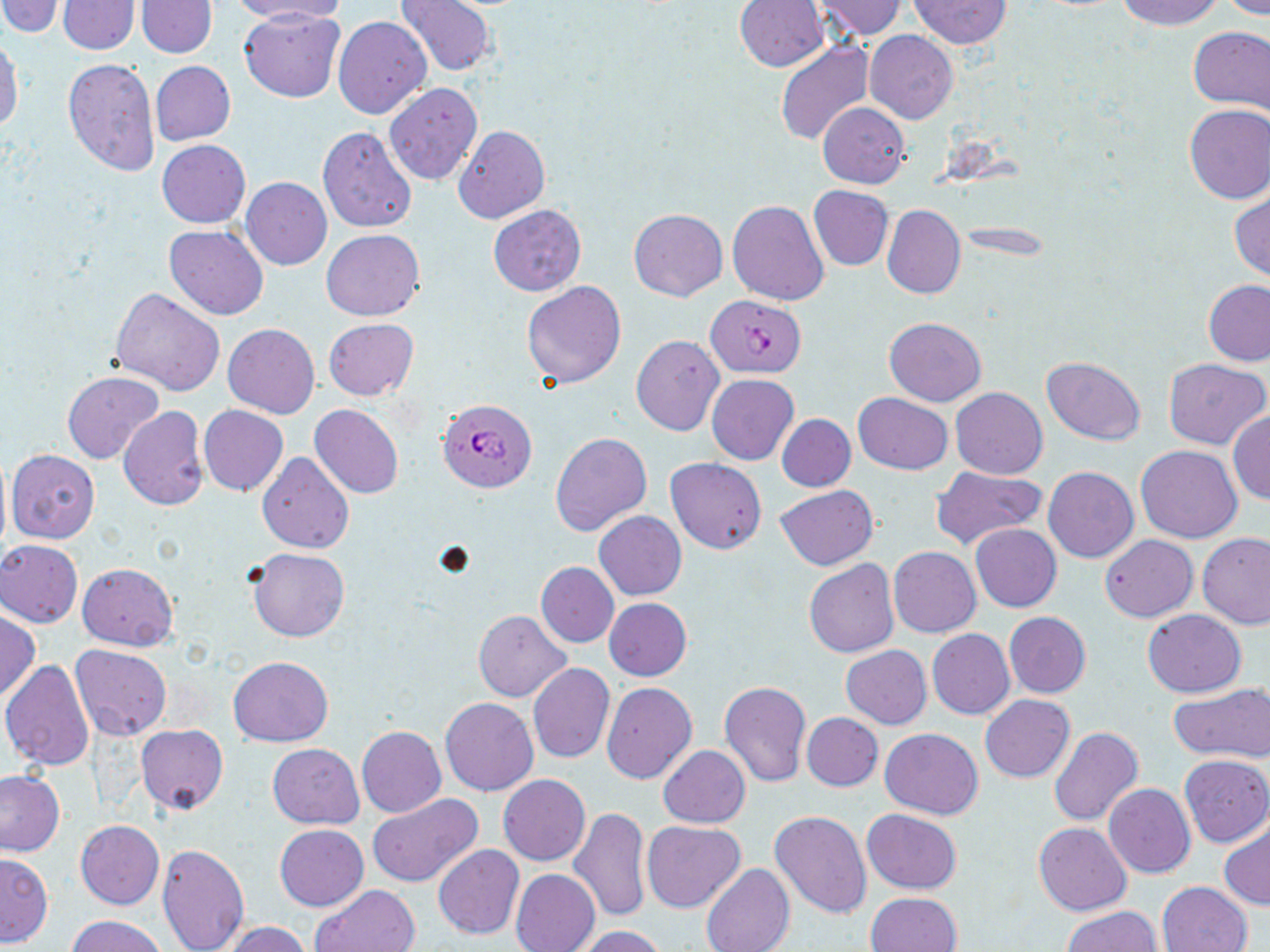
slide_level_diagnosis: Plasmodium falciparum
stain: May-Grünwald-Giemsa
uninfected_red_blood_cell_locations: 'approximate bounding boxes as (x1,y1)-(x2,y2) corner pairs in pixels: (0,0)-(65,37), (137,0)-(216,57), (233,0)-(350,24), (394,0)-(495,77), (811,0)-(906,40), (907,0)-(1012,49), (1117,0)-(1222,29), (1219,0)-(1270,19), (56,1)-(141,54), (735,1)-(828,72), (238,6)-(345,102), (333,15)-(432,119), (1188,25)-(1270,117), (865,30)-(958,124), (0,38)-(22,133), (776,39)-(875,146), (63,58)-(161,179), (150,60)-(236,145), (385,82)-(482,186), (818,102)-(909,188), (1183,104)-(1270,203), (454,125)-(550,224), (318,126)-(418,233), (157,140)-(250,228), (240,177)-(332,270), (808,185)-(893,271), (1231,190)-(1270,282), (727,201)-(828,305), (883,204)-(965,299), (488,205)-(585,296), (629,209)-(727,301), (164,226)-(269,320), (322,230)-(425,320), (1190,279)-(1268,446), (521,280)-(626,389), (1203,280)-(1270,366), (110,288)-(224,395), (884,317)-(987,406), (324,318)-(418,401), (224,323)-(320,418), (631,335)-(723,435), (1042,356)-(1145,445), (1163,358)-(1269,450), (63,371)-(164,464), (707,374)-(799,464), (951,387)-(1048,480), (854,392)-(953,475), (310,403)-(404,499), (199,405)-(288,495), (118,406)-(209,509), (1228,411)-(1270,505), (776,413)-(856,492), (549,431)-(651,538), (1137,445)-(1242,543), (0,448)-(12,559), (6,450)-(100,543), (258,451)-(354,554), (665,458)-(767,554), (930,466)-(1046,550), (1044,466)-(1138,562), (775,485)-(878,570), (594,511)-(686,600), (970,524)-(1062,612), (1197,532)-(1269,629), (1100,535)-(1197,622), (0,540)-(84,628), (889,546)-(980,637), (248,548)-(349,642), (804,559)-(899,658), (77,562)-(178,651), (536,562)-(618,648), (604,597)-(692,680), (473,609)-(571,701), (1142,609)-(1246,698), (0,610)-(40,702), (1004,612)-(1091,698), (927,629)-(1015,719), (71,645)-(172,741), (840,645)-(931,729), (228,655)-(334,746), (1,660)-(94,771), (527,663)-(615,763), (719,679)-(812,786), (602,682)-(697,784), (1170,684)-(1270,763), (980,693)-(1075,783), (439,697)-(538,795), (802,713)-(882,791), (136,724)-(228,815), (356,726)-(446,817), (1049,727)-(1143,827), (880,728)-(984,818), (266,744)-(364,829), (658,745)-(750,828), (1178,755)-(1270,847), (0,770)-(66,856), (498,774)-(590,865), (1104,783)-(1195,878), (367,795)-(481,887), (570,808)-(652,923), (863,809)-(963,894), (770,810)-(872,918), (641,820)-(746,913), (75,821)-(164,908), (1034,823)-(1131,915), (274,824)-(368,911), (1219,824)-(1270,910), (157,843)-(249,951), (433,844)-(524,939), (0,853)-(53,946), (701,864)-(795,952), (511,868)-(601,952), (1157,881)-(1253,952), (309,884)-(420,952), (865,891)-(962,952), (1064,906)-(1161,952), (67,914)-(170,952), (224,922)-(311,952), (577,926)-(667,952)'
image_size: 1270×952 pixels
field_of_view: single
magnification: 1000x
modality: optical microscopy
plasmodium_falciparum_infected_red_blood_cell_locations: 'approximate bounding boxes as (x1,y1)-(x2,y2) corner pairs in pixels: (706,295)-(806,377), (440,402)-(538,497)'
preparation: thin blood film